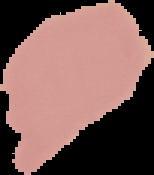

Result: negative for Plasmodium parasites. Cell region segmented out of the field of view; the surrounding area is masked to black. Image is 154×175 pixels. From a thin blood film.